Comment on the morphology of the red blood cells.
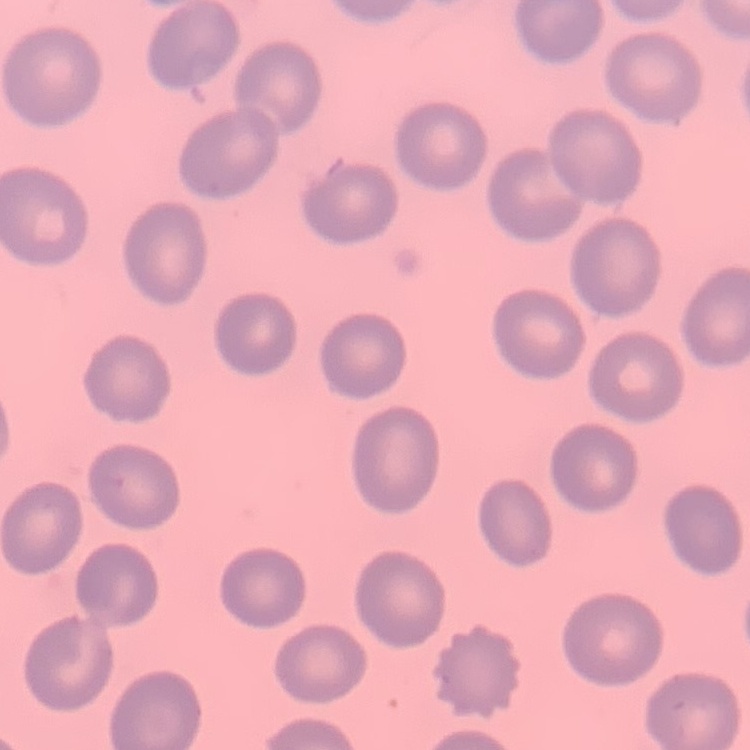

No rouleaux formation.

Summary:
  - Image type: square crop of a larger photomicrograph
  - Preparation: thin blood smear
  - Stain: Field's or Giemsa